Identify the parasite.
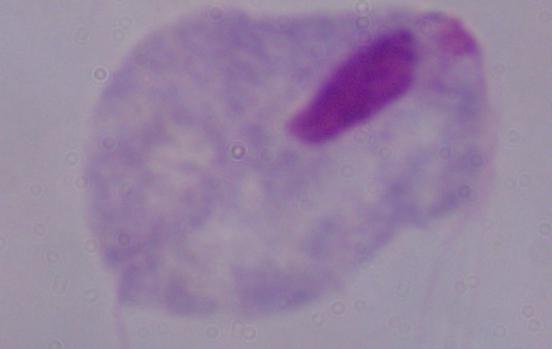
A trichomonad.

Summary:
  - Magnification: 1000x
  - Modality: photomicrograph